Give the position of every leukocyte visible.
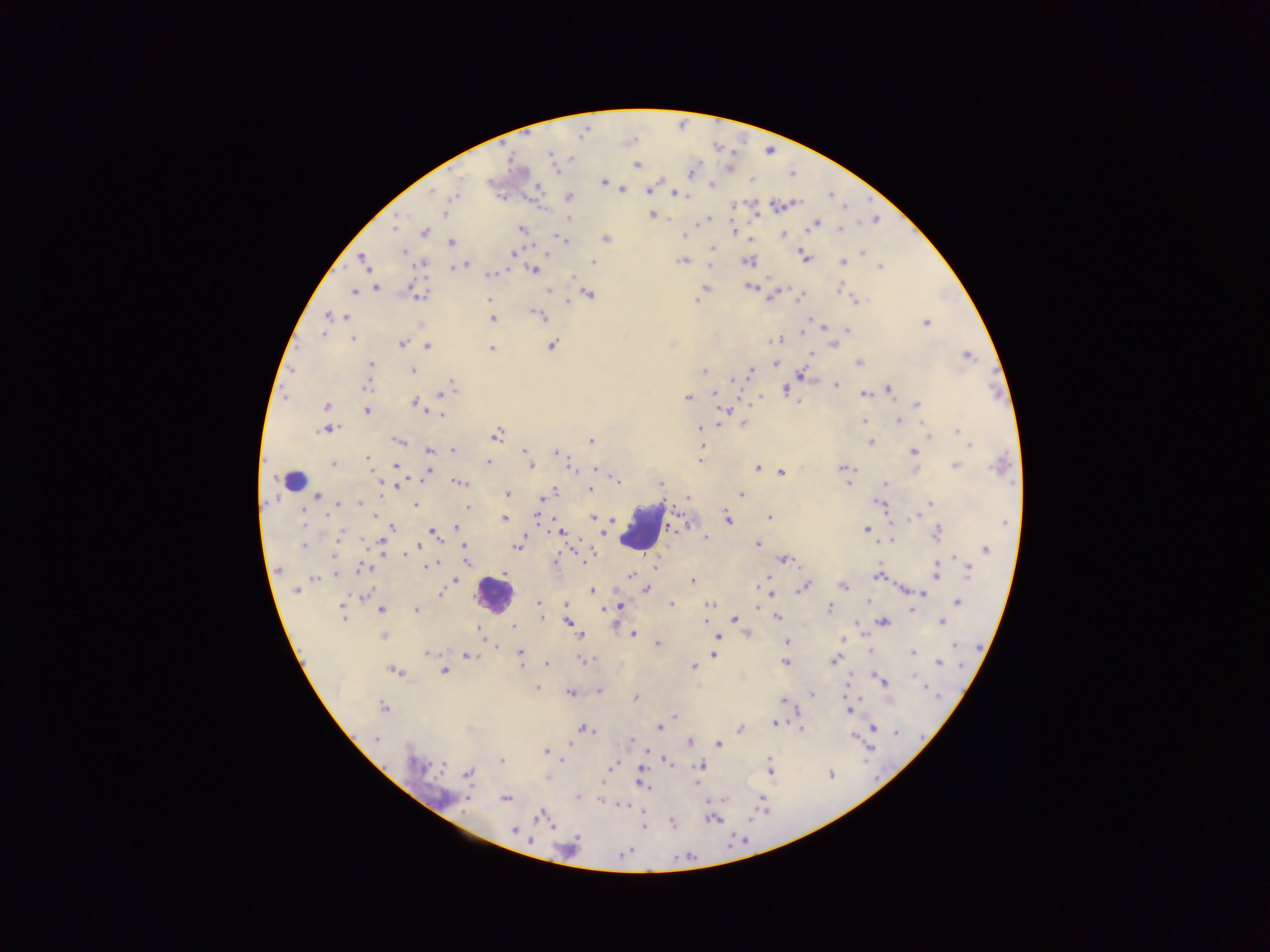
Approximate centers as {x, y} in pixels.
Leukocytes: {641, 528}, {494, 594}.
One object is labeled both malaria parasite and leukocyte by the source: {293, 480}.

Malaria parasite locations: {550, 157}, {636, 165}, {691, 172}, {751, 180}, {489, 182}, {603, 182}, {712, 184}, {537, 187}, {622, 189}, {649, 189}, {432, 191}, {677, 194}, {455, 195}, {569, 198}, {734, 205}, {776, 206}, {444, 213}, {652, 214}, {569, 220}, {705, 221}, {816, 223}, {394, 227}, {521, 228}, {840, 229}, {734, 231}, {424, 232}, {685, 235}, {784, 235}, {562, 239}, {606, 239}, {451, 243}, {712, 247}, {403, 252}, {863, 252}, {514, 254}, {806, 256}, {682, 261}, {747, 261}, {364, 262}, {843, 262}, {594, 263}, {421, 265}, {462, 265}, {456, 267}, {880, 268}, {534, 270}, {488, 275}, {572, 278}, {377, 287}, {704, 288}, {749, 288}, {839, 288}, {548, 290}, {353, 291}, {418, 292}, {589, 294}, {700, 297}, {800, 297}, {770, 298}, {489, 300}, {856, 300}, {696, 301}, {330, 316}, {339, 316}, {540, 316}, {492, 319}, {926, 323}, {847, 330}, {803, 332}, {323, 334}, {352, 339}, {775, 340}, {401, 343}, {834, 344}, {428, 346}, {552, 346}, {491, 348}, {967, 355}, {775, 363}, {859, 363}, {371, 365}, {413, 370}, {369, 371}, {703, 371}, {751, 371}, {801, 375}, {733, 378}, {451, 384}, {836, 384}, {366, 387}, {786, 390}, {890, 390}, {445, 393}, {714, 394}, {865, 395}, {688, 397}, {416, 403}, {326, 405}, {917, 405}, {367, 411}, {723, 411}, {440, 414}, {864, 421}, {899, 421}, {743, 424}, {719, 425}, {700, 427}, {327, 430}, {958, 431}, {496, 434}, {928, 434}, {966, 440}, {398, 441}, {591, 442}, {870, 442}, {701, 444}, {969, 445}, {453, 450}, {429, 451}, {524, 451}, {913, 452}, {557, 453}, {367, 459}, {701, 461}, {488, 462}, {369, 463}, {333, 465}, {396, 465}, {530, 465}, {955, 466}, {572, 467}, {757, 467}, {1000, 467}, {843, 468}, {594, 469}, {916, 470}, {429, 471}, {782, 473}, {617, 480}, {460, 483}, {847, 483}, {591, 484}, {660, 484}, {886, 484}, {397, 486}, {590, 490}, {554, 491}, {507, 494}, {741, 494}, {319, 496}, {687, 499}, {543, 501}, {359, 503}, {880, 503}, {931, 503}, {338, 504}, {415, 505}, {468, 508}, {303, 513}, {538, 515}, {375, 516}, {916, 516}, {593, 517}, {769, 517}, {504, 519}, {727, 519}, {676, 524}, {392, 526}, {456, 527}, {867, 529}, {433, 532}, {560, 532}, {936, 533}, {341, 535}, {705, 538}, {892, 540}, {757, 544}, {302, 545}, {381, 545}, {464, 545}, {417, 547}, {517, 547}, {986, 548}, {404, 554}, {786, 559}, {466, 560}, {555, 561}, {428, 566}, {656, 566}, {364, 568}, {278, 570}, {968, 571}, {937, 573}, {335, 575}, {631, 575}, {879, 576}, {314, 579}, {456, 581}, {692, 581}, {844, 586}, {803, 587}, {647, 589}, {297, 591}, {593, 591}, {921, 593}, {365, 594}, {440, 594}, {868, 602}, {538, 603}, {957, 603}, {671, 604}, {709, 604}, {566, 605}, {344, 606}, {619, 607}, {829, 608}, {415, 610}, {381, 611}, {342, 615}, {777, 617}, {542, 618}, {735, 618}, {706, 621}, {568, 622}, {884, 622}, {942, 623}, {513, 626}, {478, 629}, {633, 634}, {580, 635}, {384, 636}, {717, 639}, {787, 642}, {657, 644}, {955, 645}, {912, 652}, {427, 653}, {520, 653}, {714, 654}, {468, 656}, {586, 659}, {835, 659}, {784, 663}, {940, 663}, {547, 664}, {693, 667}, {394, 671}, {444, 671}, {915, 677}, {882, 680}, {537, 688}, {599, 691}, {570, 693}, {811, 695}, {636, 699}, {782, 700}, {383, 707}, {850, 710}, {674, 716}, {774, 723}, {585, 728}, {659, 728}, {874, 728}, {740, 729}, {801, 729}, {896, 732}, {853, 737}, {376, 738}, {630, 741}, {690, 743}, {570, 744}, {719, 744}, {545, 751}, {560, 760}, {502, 761}, {666, 761}, {417, 765}, {615, 765}, {769, 765}, {700, 766}, {468, 774}, {831, 775}, {642, 782}, {578, 798}, {505, 799}, {623, 806}, {542, 816}, {713, 819}, {673, 823}, {644, 826}, {515, 830}, {624, 854}. Thick blood smear. One field of view. Image is 1270×952 pixels. Sample from Ghana. Mobile-phone photograph taken through the microscope.